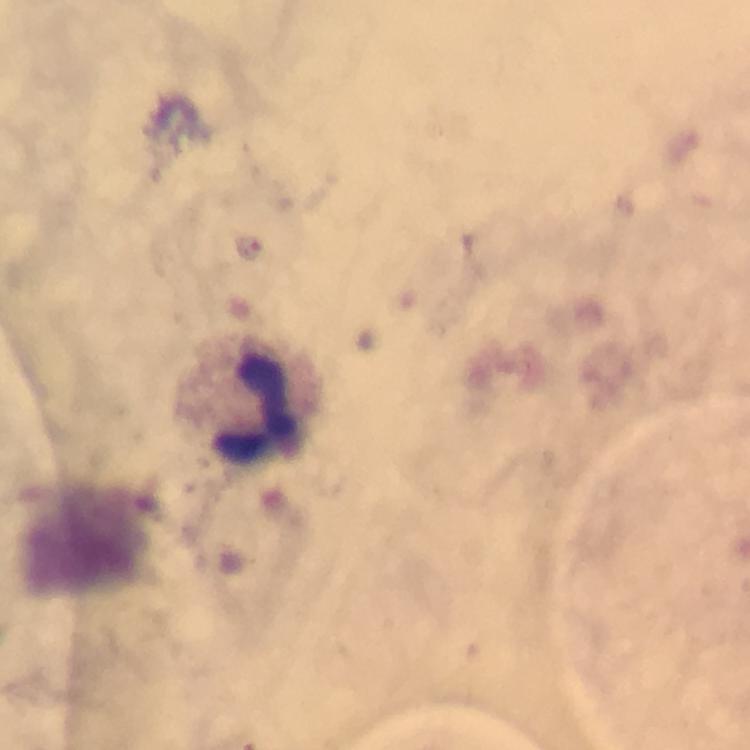 Approximate centers as [x, y] in pixels. Plasmodium parasite locations: [249, 248]. Leukocyte locations: [249, 397]. At 100x magnification. Image is 750×750 pixels. From a malaria diagnostic workup. Smartphone photograph taken through a microscope. Giemsa-stained preparation. Cropped region of a single field of view. Immersion oil was used. Thick smear.